Identify the parasite.
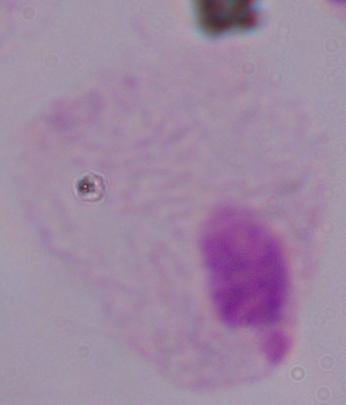
This is a trichomonad.

modality = micrograph
magnification = 1000x